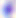

identification = Toxoplasma gondii
magnification = 400x
modality = photomicrograph